Assess the morphology of the erythrocytes.
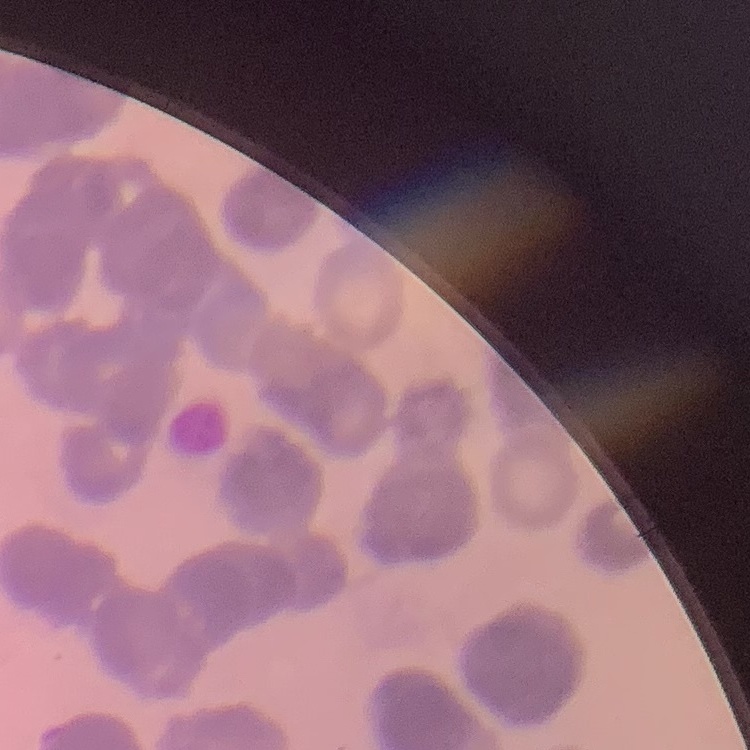

They show rouleaux formation.

Stained with either Field's or Giemsa. Square crop of a larger photomicrograph. Thin peripheral smear.